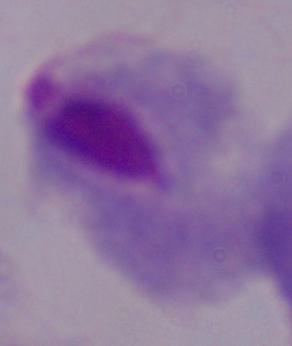
identification = trichomonad
modality = micrograph
magnification = 1000x